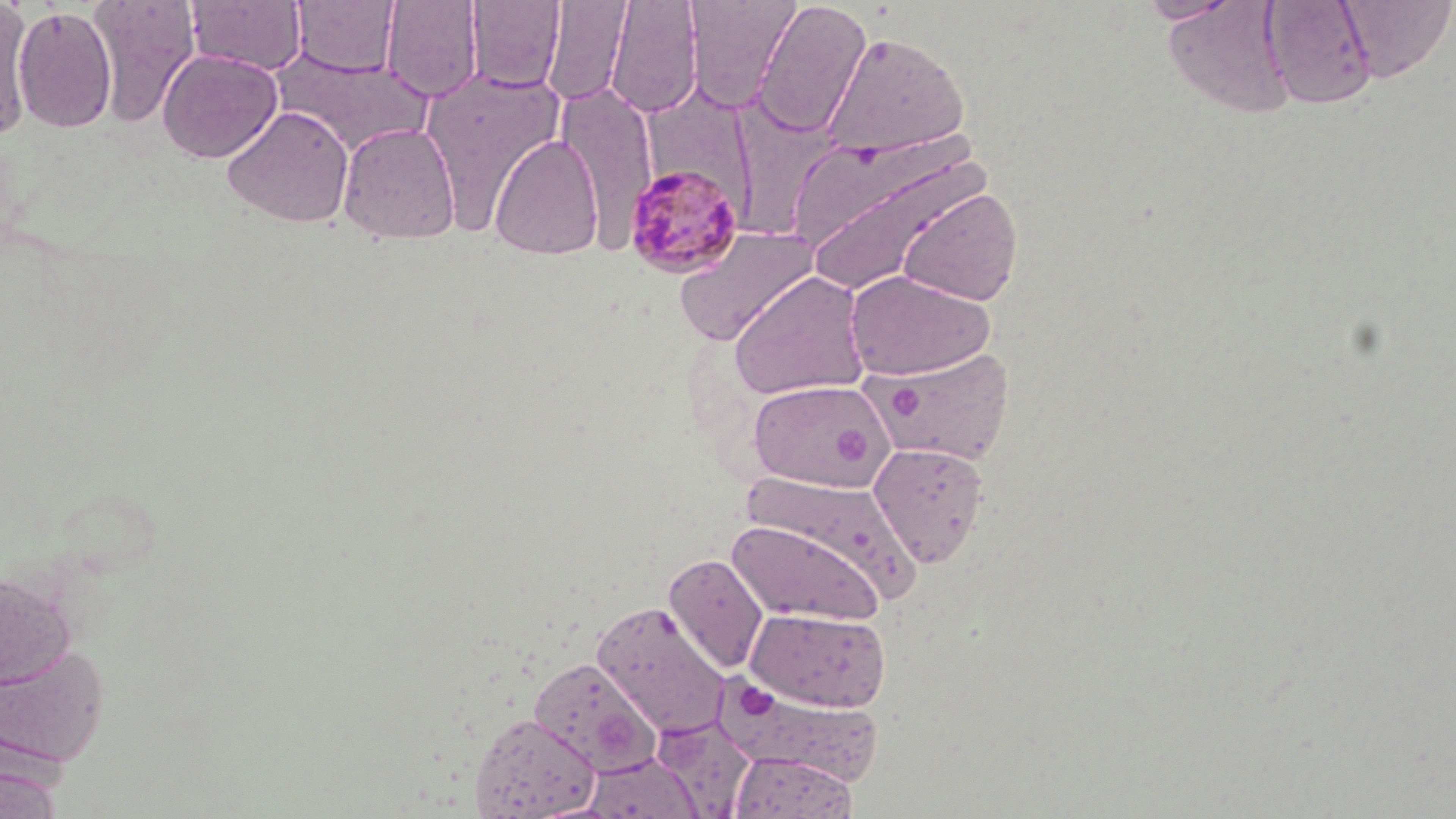 Approximate bounding boxes as (x1,y1)-(x2,y2) corner pairs in pixels. Platelet locations: (890,388)-(922,422), (833,424)-(873,465), (739,683)-(780,719). Plasmodium malariae-infected red blood cell locations: (623,163)-(745,278). Uninfected red blood cell locations: (88,0)-(201,127), (185,0)-(307,75), (291,0)-(400,76), (381,0)-(483,102), (467,0)-(565,91), (605,0)-(704,118), (685,0)-(802,111), (753,0)-(872,138), (1136,0)-(1243,24), (1162,0)-(1304,120), (1260,0)-(1377,110), (1337,0)-(1456,81), (0,1)-(35,137), (542,1)-(633,107), (13,6)-(117,133), (824,30)-(970,159), (158,49)-(282,163), (274,51)-(435,155), (419,67)-(568,230), (558,83)-(658,247), (733,101)-(847,235), (221,105)-(354,228), (338,122)-(461,244), (490,134)-(603,259), (798,139)-(994,298), (898,187)-(1022,306), (673,225)-(820,346), (846,270)-(994,380), (728,271)-(870,400), (870,345)-(1012,466), (747,379)-(892,491), (868,441)-(990,568), (736,471)-(920,603), (727,518)-(884,627), (663,553)-(769,674), (0,572)-(75,691), (592,601)-(733,737), (745,607)-(892,712), (0,642)-(110,769), (527,656)-(661,775), (714,676)-(882,784), (469,712)-(600,818), (650,715)-(755,817), (728,751)-(857,819), (582,752)-(703,819), (0,764)-(64,819). Slide-level diagnosis: Plasmodium malariae. Thin blood film. One field of a larger specimen. Optical microscopy. 1000x magnification. May-Grünwald-Giemsa-stained preparation. Image is 1456×819 pixels.